Report the malaria status of this cell.
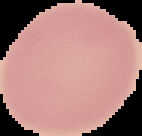
Uninfected.

From a thin blood film. Image is 142×136 pixels. The area outside the segmented cell region is set to black.